Identify the parasite.
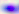
This is Toxoplasma gondii.

Summary:
  - Modality: photomicrograph
  - Magnification: 400x